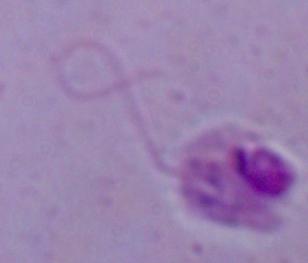

Summary:
  - Modality: photomicrograph
  - Magnification: 1000x
  - Identification: Leishmania